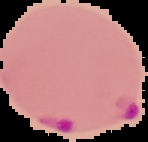

Summary:
  - Image size: 148×142 pixels
  - Image type: segmented cell region with the area outside set to black
  - Malaria status: parasitized
  - Preparation: thin blood smear